Comment on the morphology of the red blood cells.
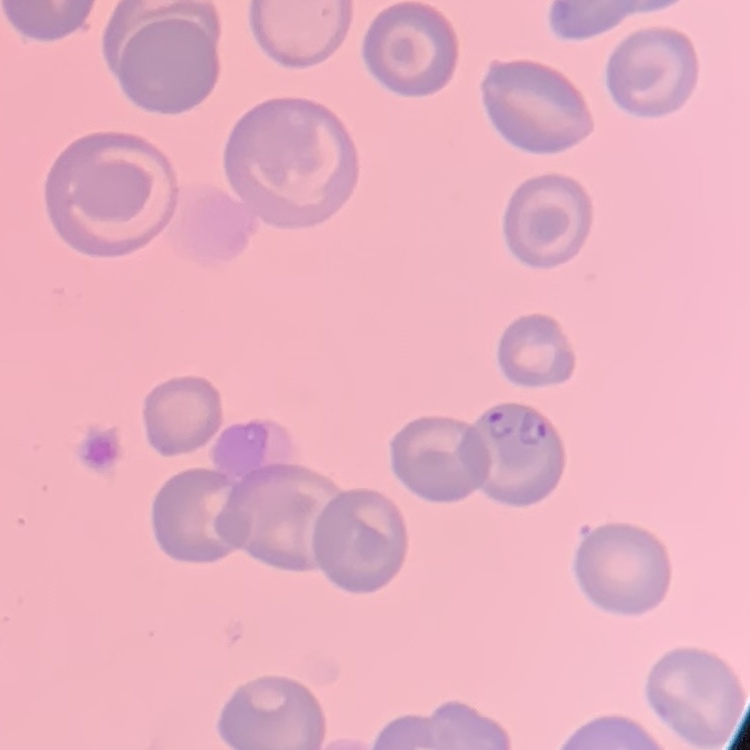
They show no rouleaux formation.

One tile cut from a larger photomicrograph. Field's or Giemsa stain. Thin blood film.